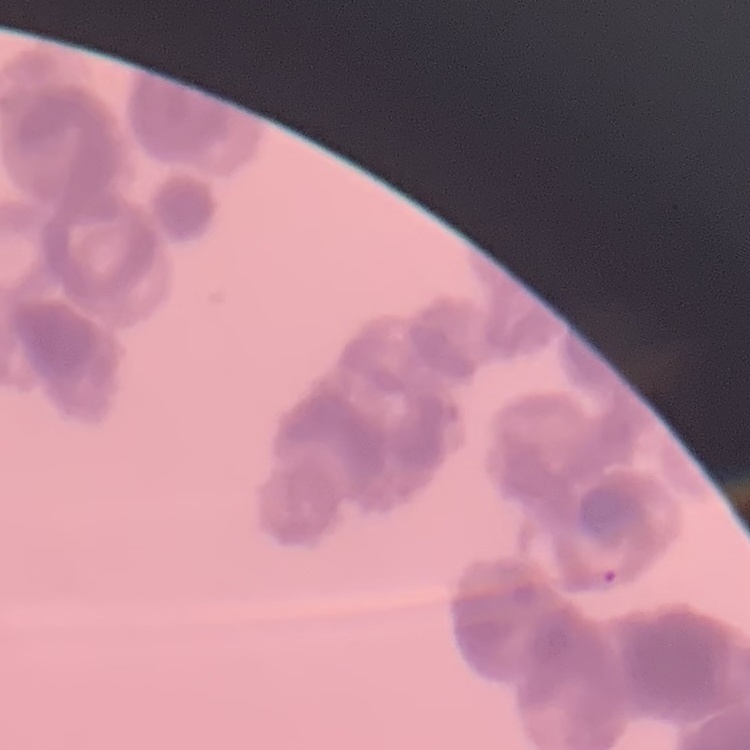 The erythrocytes exhibit rouleaux formation. Thin blood film. Stained with either Field's or Giemsa. One tile cut from a larger photomicrograph.